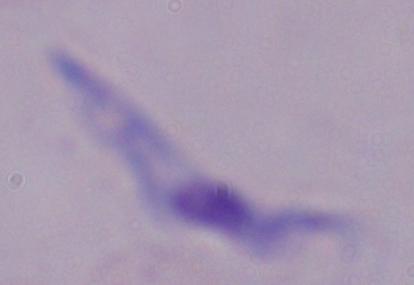

{
  "identification": "trypanosome",
  "modality": "micrograph",
  "magnification": "1000x"
}